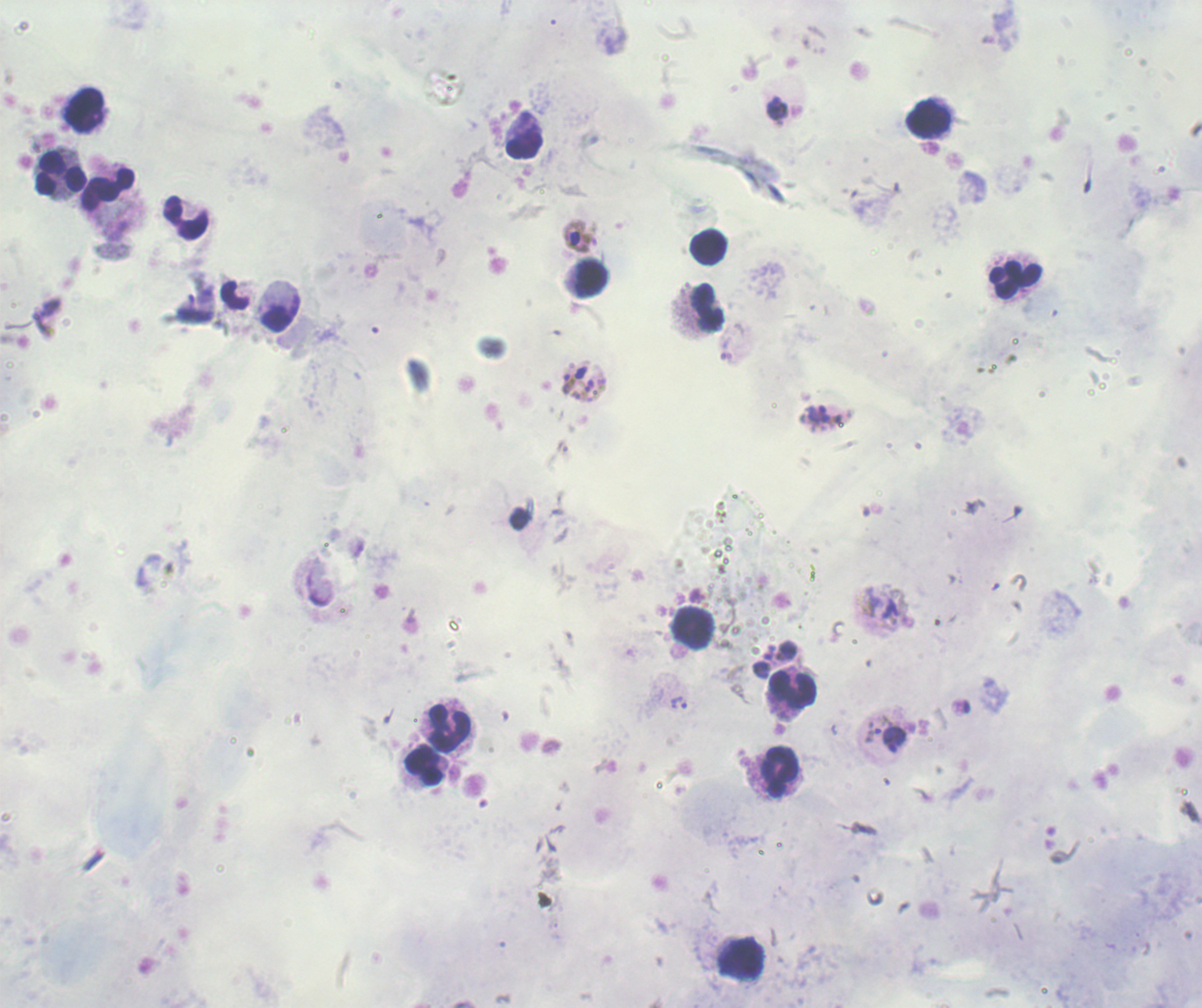
Approximate object centers, in pixels from the top-left corner.
Summary:
  - Gametocyte locations: (x=578, y=237), (x=575, y=377)
  - Trophozoite locations: (x=777, y=108), (x=817, y=417), (x=679, y=703), (x=873, y=733), (x=895, y=739)
  - Leukocyte locations: (x=84, y=108), (x=929, y=121), (x=523, y=136), (x=60, y=173), (x=109, y=192), (x=187, y=219), (x=709, y=247), (x=586, y=279), (x=1016, y=280), (x=235, y=293), (x=279, y=306), (x=700, y=311), (x=693, y=627), (x=793, y=689), (x=449, y=726), (x=423, y=765), (x=780, y=772), (x=742, y=959)
  - Life-cycle stages observed: trophozoite, gametocyte
  - Field of view: one from this slide
  - Background quality: poor
  - Image size: 1202×1008 pixels
  - Context: previously used in a real diagnosis
  - Preparation: thick smear of blood
  - Result: Plasmodium parasites identified
  - Stain: Romanowsky
  - Magnification: 100x